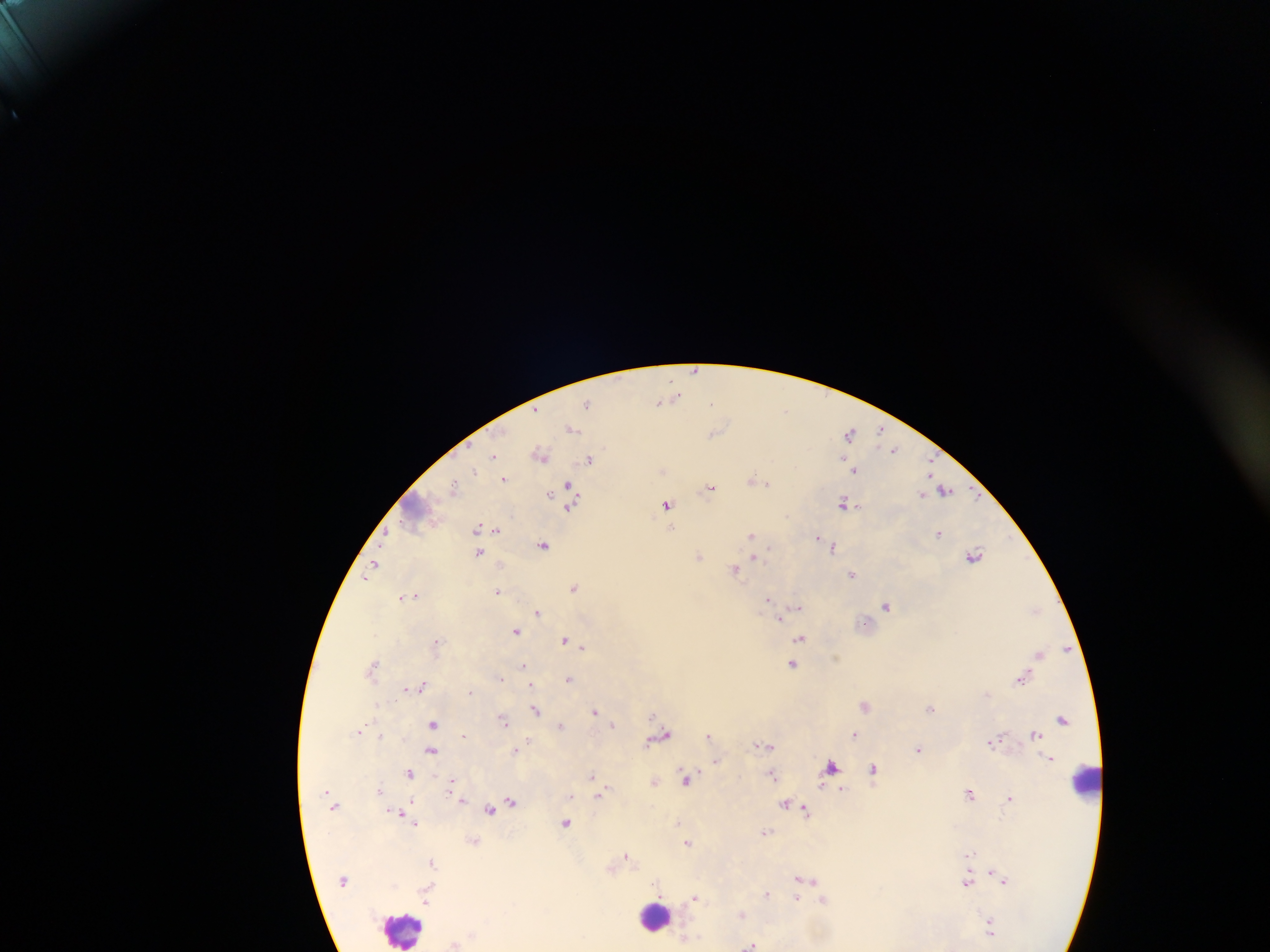
country = Ghana
capture = mobile-phone photograph through a microscope
leukocyte locations = approximate centers as x y in pixels: 1085 779; 654 917; 404 928
field of view = single
Plasmodium parasite locations = approximate centers as x y in pixels: 696 370; 674 397; 660 401; 587 403; 712 404; 785 410; 572 429; 849 432; 881 432; 714 433; 893 450; 540 453; 493 456; 589 458; 854 470; 475 471; 504 478; 756 479; 454 487; 710 487; 567 490; 944 490; 844 503; 667 504; 477 527; 672 528; 497 530; 752 534; 939 534; 819 538; 824 542; 544 545; 831 546; 479 552; 974 555; 698 556; 754 557; 372 567; 735 569; 853 574; 367 577; 573 587; 498 591; 412 596; 404 597; 768 600; 798 606; 886 606; 1035 610; 539 612; 780 617; 515 631; 800 639; 564 640; 437 642; 582 646; 1040 654; 373 665; 524 665; 792 665; 500 678; 569 678; 1021 678; 530 684; 422 686; 406 688; 471 693; 865 705; 931 708; 536 710; 595 711; 1063 719; 504 721; 433 724; 612 724; 562 725; 360 730; 1035 733; 855 734; 463 735; 709 736; 660 737; 528 741; 992 741; 766 745; 517 749; 919 749; 430 751; 715 761; 831 767; 874 771; 410 773; 591 776; 772 776; 687 778; 654 782; 452 784; 379 789; 603 791; 969 793; 1010 797; 510 802; 786 804; 490 810; 806 810; 678 822; 566 823; 415 824; 767 832; 687 842; 971 853; 626 856; 431 862; 994 873; 803 879; 1003 879; 967 882; 767 894; 425 898; 695 898; 796 900; 824 900; 991 928; 752 945
image size = 1270×952 pixels
preparation = thick blood smear